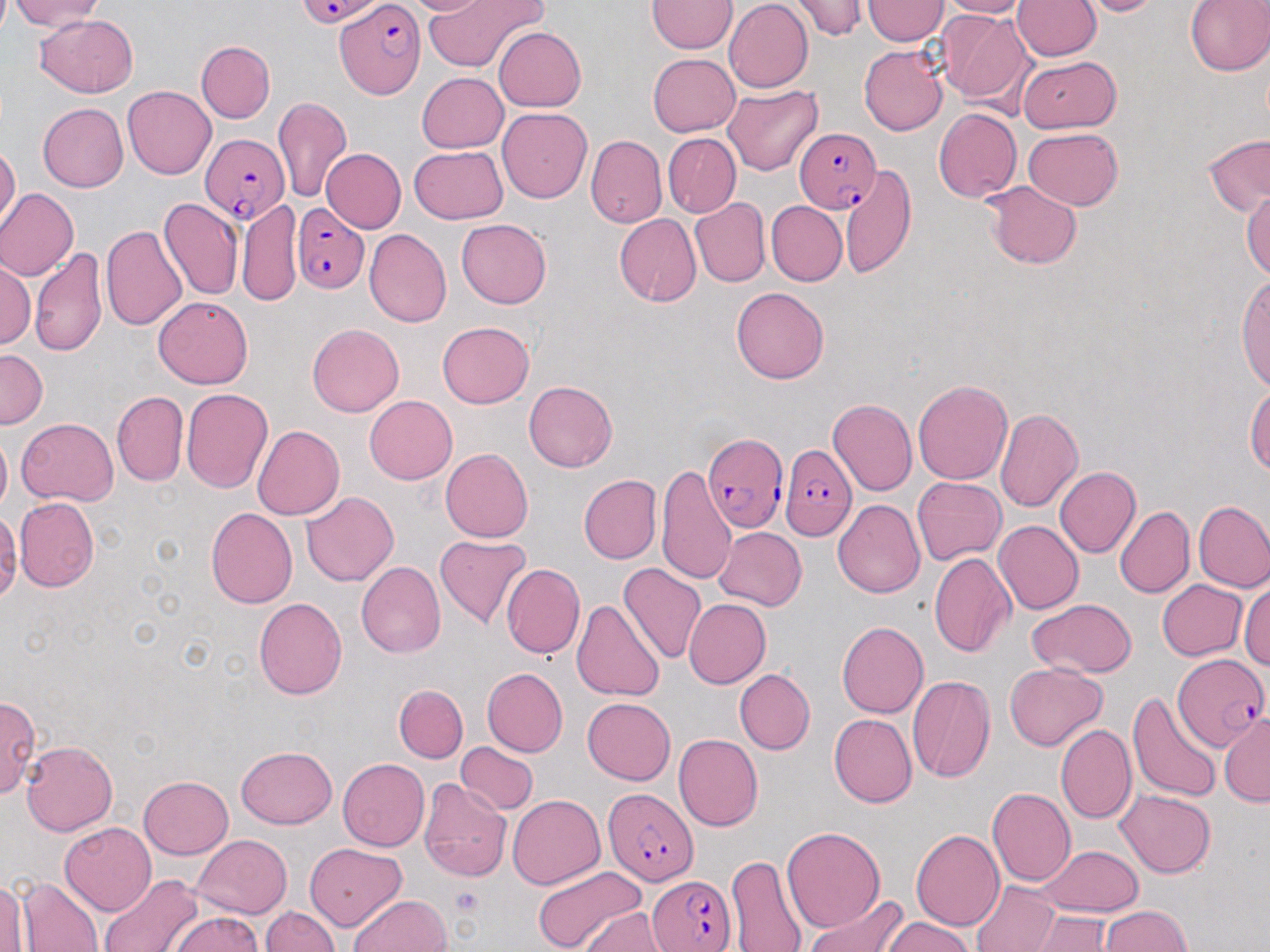 Approximate bounding boxes as [x1, y1, x2, y2] in pixels. Uninfected red blood cell locations: [398, 0, 497, 16], [423, 0, 546, 73], [724, 0, 812, 92], [787, 0, 867, 41], [863, 0, 949, 45], [939, 0, 1032, 19], [1013, 0, 1101, 60], [1076, 0, 1162, 17], [1184, 0, 1270, 76], [11, 1, 105, 31], [646, 1, 737, 53], [937, 9, 1035, 110], [36, 14, 138, 97], [495, 27, 586, 112], [196, 41, 274, 122], [859, 45, 949, 136], [648, 53, 741, 137], [1017, 56, 1121, 133], [417, 72, 507, 152], [722, 84, 822, 176], [123, 85, 216, 179], [273, 96, 353, 202], [38, 102, 127, 192], [498, 107, 592, 203], [933, 109, 1022, 202], [1023, 127, 1123, 210], [663, 133, 741, 217], [1203, 133, 1270, 217], [585, 135, 667, 228], [0, 144, 20, 232], [409, 146, 508, 225], [321, 148, 406, 233], [839, 164, 917, 277], [982, 181, 1082, 269], [1241, 186, 1270, 281], [0, 188, 78, 281], [158, 197, 242, 301], [690, 198, 770, 288], [236, 199, 301, 308], [765, 201, 846, 286], [614, 214, 701, 306], [457, 219, 551, 309], [100, 224, 188, 331], [364, 229, 452, 328], [30, 247, 107, 358], [1, 257, 35, 350], [1236, 273, 1270, 390], [731, 286, 829, 384], [154, 295, 252, 389], [437, 321, 535, 408], [307, 324, 403, 416], [0, 349, 49, 429], [912, 379, 1012, 485], [524, 380, 617, 471], [1246, 383, 1270, 475], [181, 388, 272, 492], [112, 391, 188, 487], [364, 395, 457, 484], [828, 398, 917, 496], [995, 407, 1083, 513], [18, 417, 117, 506], [252, 426, 345, 520], [0, 430, 11, 516], [440, 448, 533, 542], [655, 464, 737, 586], [1054, 466, 1140, 558], [579, 475, 661, 565], [912, 477, 1006, 565], [300, 491, 398, 587], [14, 497, 99, 593], [833, 499, 925, 598], [1193, 500, 1270, 592], [1115, 506, 1194, 598], [207, 508, 298, 608], [0, 513, 20, 600], [994, 520, 1084, 615], [713, 527, 806, 610], [434, 534, 531, 629], [929, 553, 1015, 658], [356, 561, 446, 658], [618, 562, 706, 664], [501, 563, 585, 659], [1157, 579, 1247, 660], [1240, 582, 1270, 669], [253, 597, 348, 699], [1026, 598, 1138, 678], [571, 599, 665, 703], [683, 599, 771, 689], [837, 622, 929, 719], [862, 640, 960, 756], [1004, 661, 1106, 751], [482, 668, 568, 757], [734, 670, 815, 754], [907, 674, 997, 783], [393, 684, 469, 762], [1127, 691, 1222, 803], [0, 695, 40, 800], [582, 697, 676, 785], [1218, 713, 1269, 806], [829, 714, 917, 808], [1102, 721, 1206, 823], [1055, 723, 1136, 824], [673, 733, 763, 831], [455, 740, 538, 815], [21, 741, 117, 836], [235, 747, 337, 829], [338, 759, 429, 851], [139, 776, 233, 859], [419, 777, 511, 882], [987, 787, 1076, 887], [1116, 789, 1216, 877], [508, 794, 605, 889], [59, 821, 156, 916], [781, 825, 885, 933], [910, 829, 1004, 930], [192, 834, 291, 918], [305, 844, 406, 931], [1036, 845, 1143, 917], [725, 854, 808, 951], [533, 864, 645, 952], [98, 873, 202, 952], [13, 876, 105, 951], [0, 878, 28, 950], [970, 880, 1060, 952], [349, 894, 452, 952], [802, 895, 907, 952], [1099, 905, 1191, 951], [259, 906, 339, 952], [580, 909, 673, 952], [1032, 911, 1115, 951], [167, 912, 267, 952], [879, 917, 975, 952]. Platelet locations: [449, 886, 483, 917]. Plasmodium falciparum-infected red blood cell locations: [297, 0, 386, 27], [334, 2, 424, 100], [793, 128, 881, 213], [200, 133, 288, 224], [291, 203, 369, 294], [704, 433, 788, 532], [779, 443, 857, 539], [1173, 654, 1265, 754], [602, 788, 698, 885], [646, 874, 737, 950]. Slide-level diagnosis: Plasmodium falciparum. May-Grünwald-Giemsa-stained preparation. Light microscopy. One field of a larger specimen. 1000x magnification. Thin blood smear. Image is 1270×952 pixels.